Assess the morphology of the red blood cells.
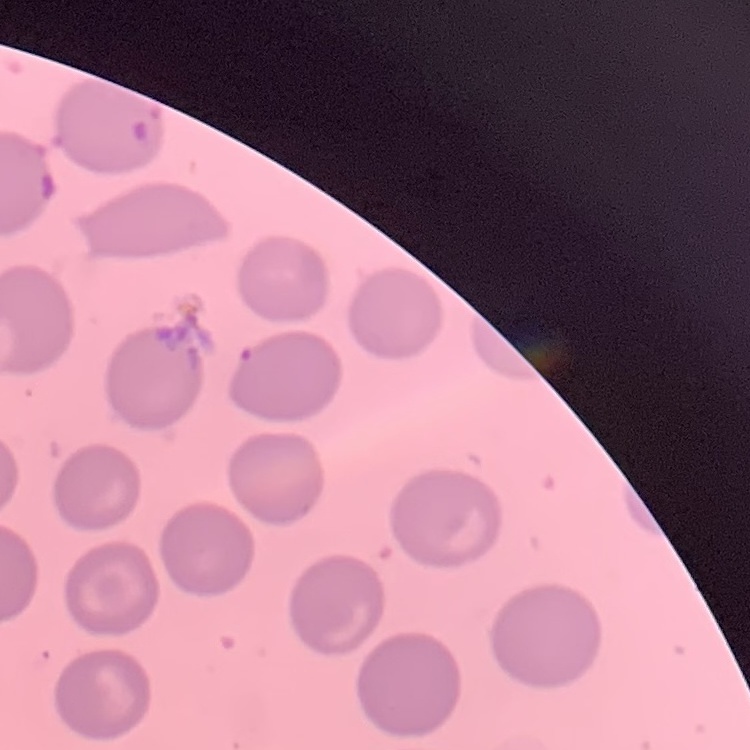
They show no rouleaux formation.

{
  "image_type": "one tile cut from a larger photomicrograph",
  "stain": "Field's or Giemsa",
  "preparation": "thin blood smear"
}